Comment on the morphology of the erythrocytes.
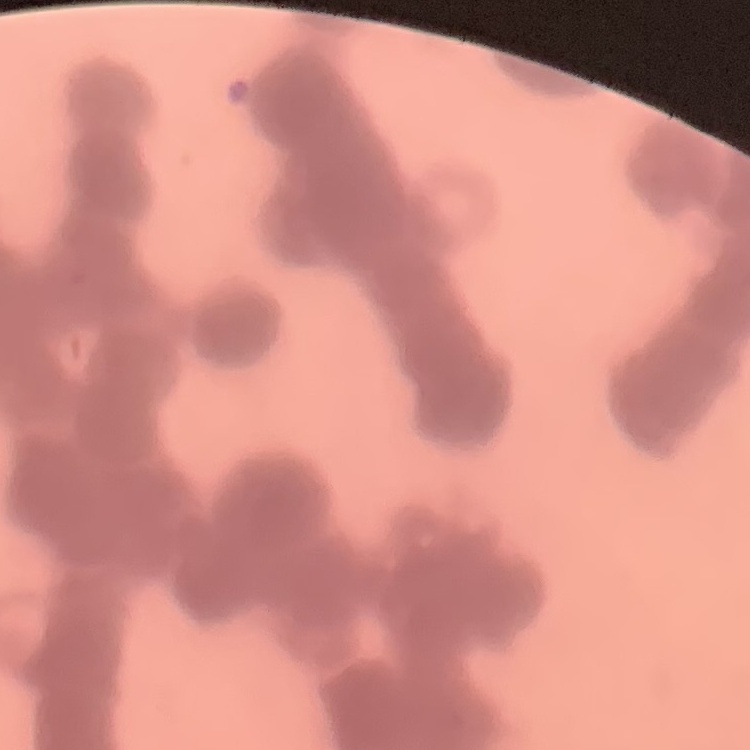
They show rouleaux formation.

Thin peripheral smear. One tile cut from a larger photomicrograph. Stained with either Field's or Giemsa.